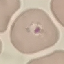

Result: malaria parasites detected. Photographed with a smartphone camera at the microscope eyepiece. Thin smear of blood. Cell patch, automatically extracted from a larger field of view and resized to 64 × 64 pixels. Giemsa-stained preparation.